Locate every blood parasite and identify its species.
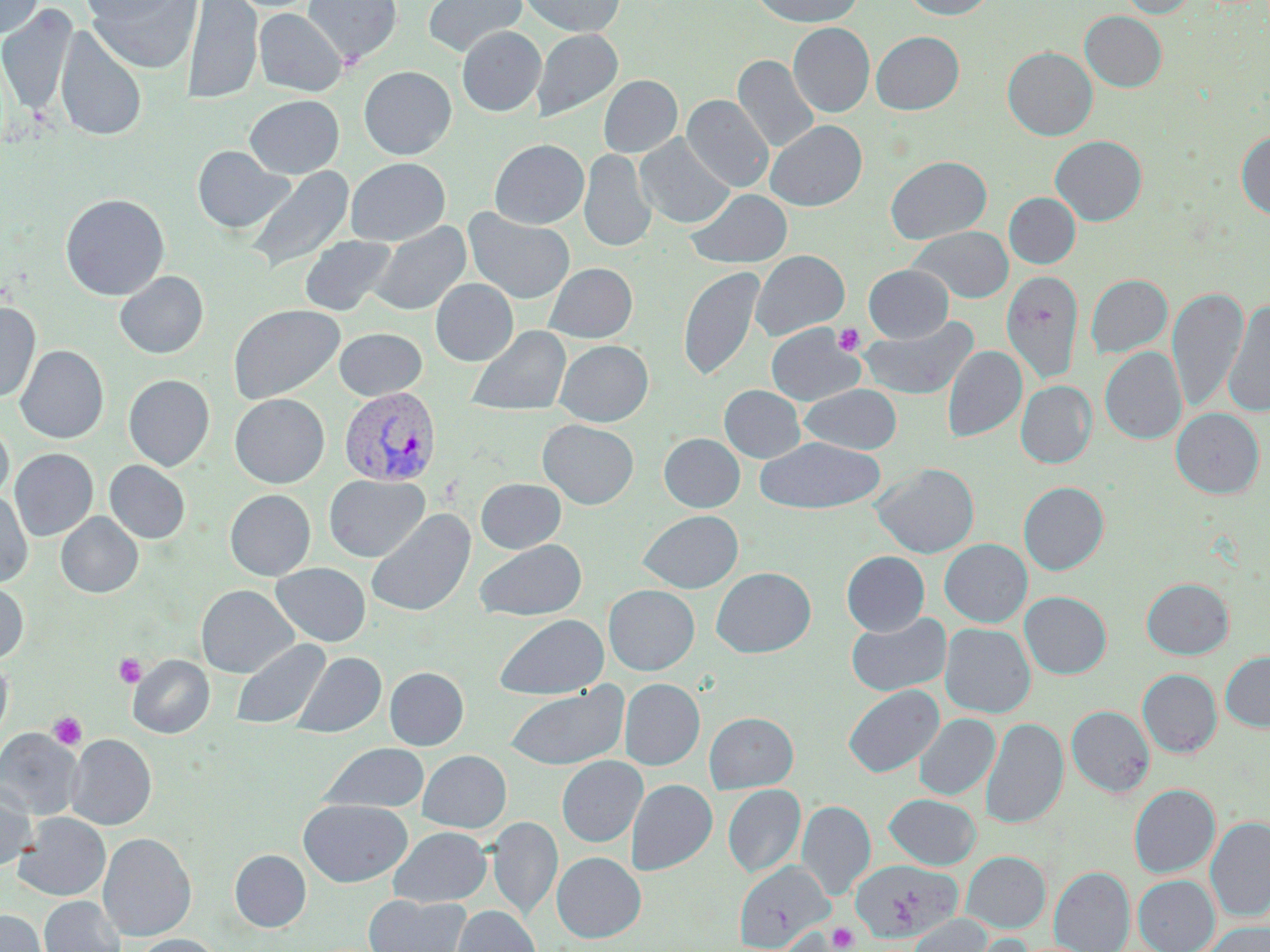

Approximate bounding boxes as (x1,y1)-(x2,y2) corner pairs in pixels.
Plasmodium vivax-infected red blood cells: (338,385)-(442,486).
No Plasmodium falciparum, Plasmodium ovale, Plasmodium malariae, Babesia divergens, or Trypanosoma brucei observed.

Summary:
  - Platelet locations: (833,323)-(865,356), (113,653)-(146,688), (48,712)-(86,750), (827,923)-(858,951)
  - Uninfected red blood cell locations: (85,0)-(201,74), (182,0)-(263,105), (303,0)-(402,65), (423,0)-(526,57), (518,0)-(625,36), (751,0)-(864,27), (901,0)-(997,20), (1118,0)-(1197,18), (0,1)-(44,38), (79,1)-(185,25), (0,4)-(77,115), (254,7)-(347,96), (1080,11)-(1167,92), (788,23)-(874,117), (55,25)-(147,142), (457,27)-(545,116), (532,28)-(622,121), (871,31)-(964,115), (1003,47)-(1097,140), (733,54)-(819,153), (359,66)-(457,160), (599,75)-(682,157), (245,95)-(344,179), (683,95)-(774,193), (765,120)-(867,211), (1236,131)-(1270,221), (635,134)-(734,228), (1050,135)-(1147,225), (489,139)-(589,229), (192,145)-(293,233), (579,149)-(656,252), (885,155)-(992,244), (345,157)-(450,246), (244,166)-(354,274), (685,189)-(792,268), (1004,192)-(1080,269), (60,193)-(170,300), (464,209)-(575,304), (369,222)-(471,316), (909,226)-(1014,303), (299,236)-(397,316), (750,250)-(850,341), (544,263)-(637,343), (864,265)-(953,342), (678,266)-(765,382), (1001,270)-(1083,385), (114,271)-(209,359), (1086,274)-(1172,358), (430,278)-(518,366), (1168,285)-(1247,414), (1222,300)-(1270,418), (0,302)-(41,403), (228,304)-(345,404), (857,315)-(979,401), (766,323)-(864,406), (466,325)-(571,417), (333,327)-(427,401), (554,340)-(653,426), (15,345)-(108,443), (942,345)-(1027,442), (1100,347)-(1186,444), (123,374)-(215,471), (1016,380)-(1096,468), (800,384)-(902,454), (719,385)-(805,463), (230,394)-(330,488), (1170,408)-(1265,499), (538,419)-(639,509), (0,420)-(13,503), (659,434)-(745,512), (755,437)-(885,514), (10,448)-(98,540), (105,460)-(190,543), (873,463)-(979,558), (323,474)-(429,562), (476,478)-(566,553), (1018,482)-(1108,575), (225,489)-(316,580), (0,490)-(33,588), (366,509)-(476,618), (639,510)-(743,593), (56,512)-(143,598), (474,539)-(587,620), (939,539)-(1032,627), (841,551)-(929,635), (271,563)-(371,646), (711,567)-(816,657), (1141,578)-(1234,659), (0,580)-(29,664), (196,585)-(298,678), (603,585)-(699,675), (1020,591)-(1111,679), (846,612)-(951,696), (494,614)-(609,699), (940,623)-(1035,717), (231,638)-(331,729), (292,651)-(386,738), (1220,651)-(1270,731), (0,654)-(13,747), (128,655)-(214,738), (384,667)-(468,750), (1138,669)-(1222,757), (619,678)-(705,770), (843,684)-(944,777), (505,685)-(629,770), (1066,706)-(1154,797), (704,712)-(798,792), (915,713)-(999,800), (981,717)-(1068,829), (0,728)-(83,820), (66,734)-(156,830), (319,742)-(429,814), (418,750)-(511,833), (557,756)-(647,846), (626,779)-(717,875), (0,780)-(36,871), (723,784)-(805,877), (1129,784)-(1220,877), (884,793)-(981,869), (299,799)-(412,887), (797,800)-(875,899), (14,813)-(111,901), (487,816)-(562,922), (1205,817)-(1270,920), (388,826)-(491,907), (98,832)-(196,941), (230,850)-(311,932), (962,851)-(1050,934), (552,852)-(646,942), (851,859)-(962,944), (734,861)-(833,951), (1050,866)-(1134,952), (1133,875)-(1219,952), (364,894)-(470,952), (39,896)-(125,952), (451,905)-(540,952), (0,909)-(47,952), (908,914)-(995,952), (1201,922)-(1270,952), (132,934)-(222,952)
  - Slide-level diagnosis: Plasmodium vivax
  - Preparation: thin blood film
  - Modality: light microscopy
  - Stain: May-Grünwald-Giemsa
  - Image size: 1270×952 pixels
  - Magnification: 1000x
  - Field of view: single